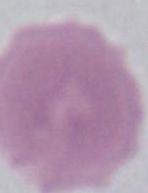

identification = erythrocyte
modality = micrograph
magnification = 1000x